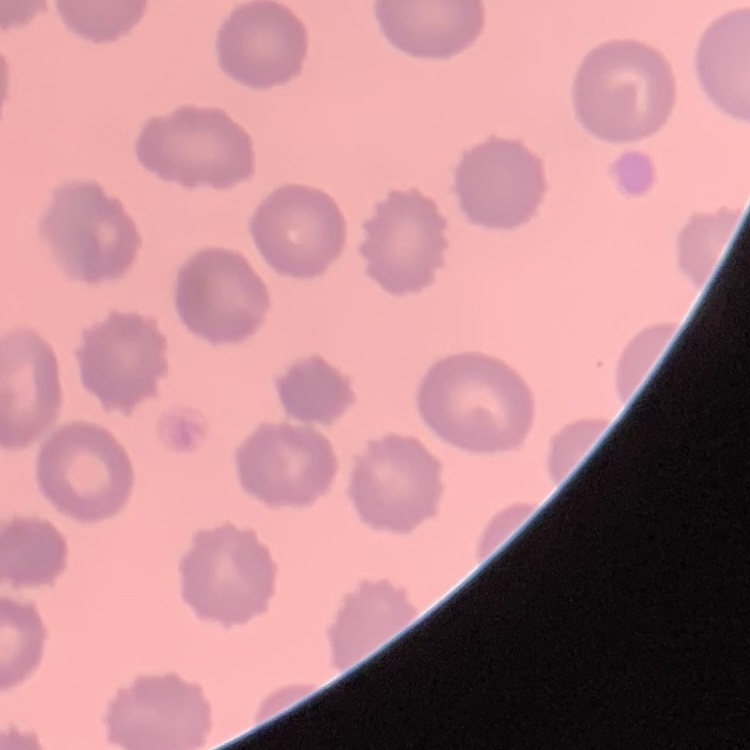
Summary:
  - Red blood cell morphology: no rouleaux formation
  - Stain: Field's or Giemsa
  - Image type: one tile cut from a larger photomicrograph
  - Preparation: thin blood film